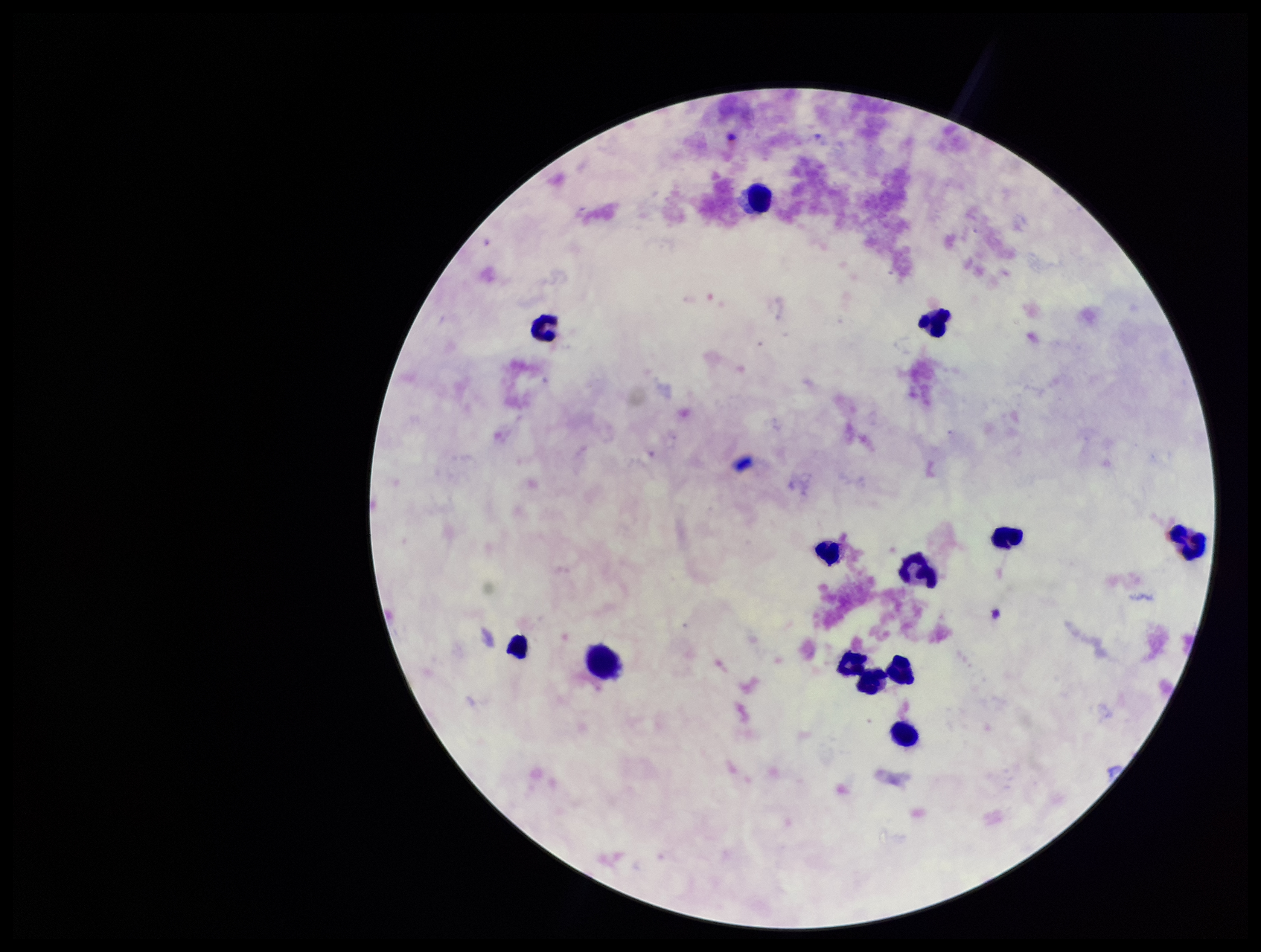
Summary:
  - Capture: smartphone photograph through the microscope eyepiece
  - Stain: Giemsa
  - Patient malaria status: negative
  - Leukocyte count: 13
  - Field of view: single
  - Plasmodium parasites: none seen
  - Parasite count: 0
  - Preparation: thick smear
  - Image size: 1261×952 pixels